Classify this cell by malaria status.
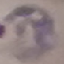
Parasitized.

Photographed with a smartphone camera at the microscope eyepiece. Thin smear of blood. Cell patch, automatically extracted from a larger field of view and resized to 64 × 64 pixels. Giemsa stain.